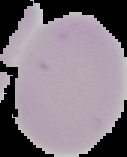
Summary:
  - Result: no Plasmodium parasites seen
  - Preparation: thin blood smear
  - Image type: segmented cell region on a black background
  - Image size: 127×157 pixels